Assess this cell for malaria.
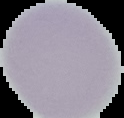
It is uninfected.

preparation: thin blood smear
image_size: 124×118 pixels
image_type: cell region segmented out of the field of view; surrounding area masked to black